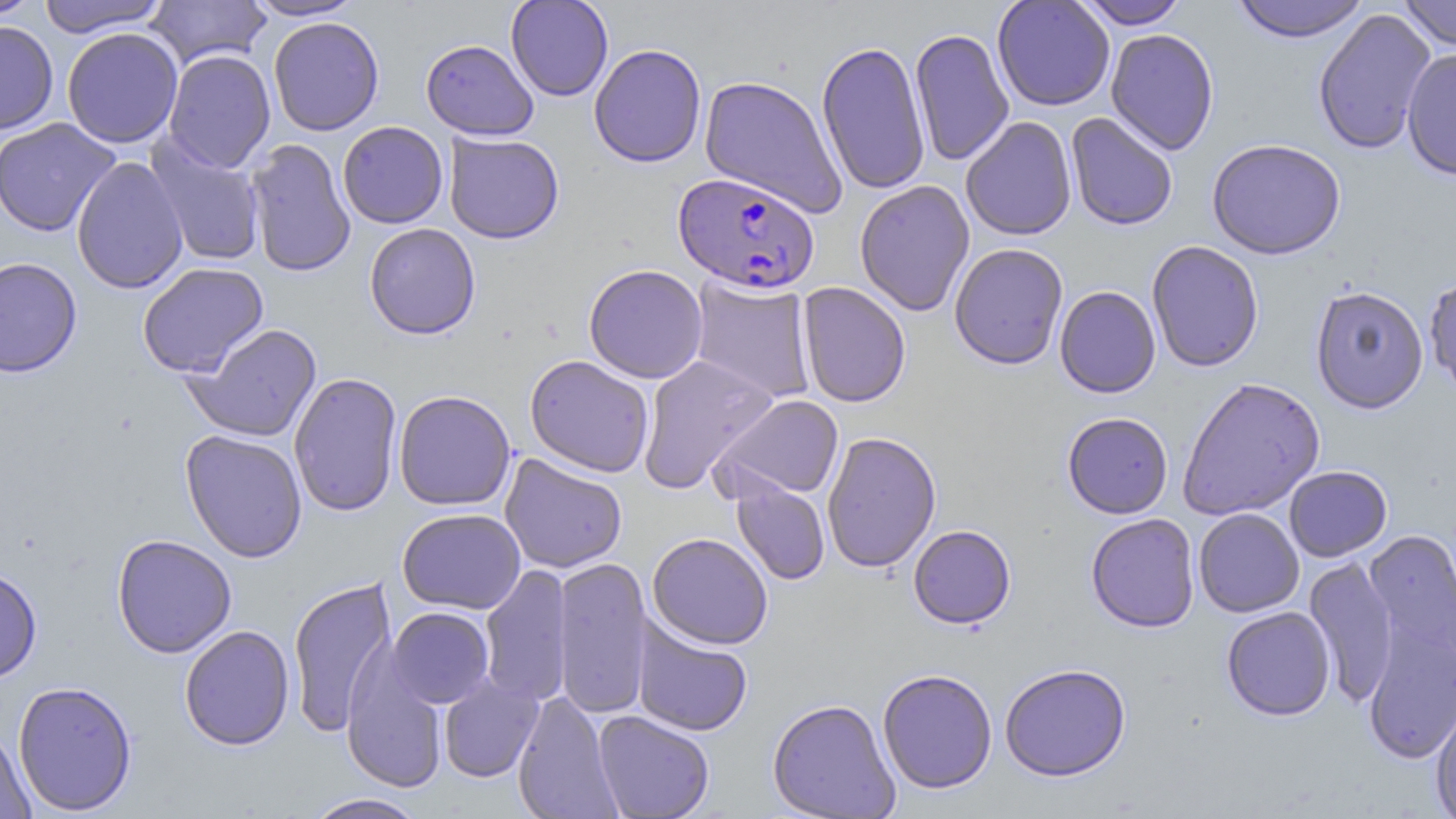
Approximate bounding boxes as (x1, y1, x2, y2) in pixels. Uninfected red blood cell locations: (0, 0, 43, 22), (37, 0, 170, 38), (243, 0, 365, 21), (505, 0, 614, 102), (992, 0, 1115, 111), (1074, 0, 1191, 29), (1230, 0, 1370, 43), (1399, 0, 1456, 50), (146, 1, 271, 70), (1313, 8, 1436, 155), (268, 17, 384, 136), (0, 21, 58, 135), (62, 27, 183, 149), (909, 27, 1015, 167), (1105, 28, 1220, 155), (420, 39, 539, 140), (817, 40, 931, 197), (589, 43, 707, 168), (1401, 48, 1456, 180), (163, 49, 276, 173), (699, 74, 847, 218), (1065, 112, 1178, 231), (959, 116, 1077, 241), (0, 118, 120, 237), (337, 121, 449, 229), (443, 132, 565, 244), (145, 135, 266, 268), (245, 138, 356, 278), (1207, 138, 1346, 260), (71, 156, 189, 295), (854, 180, 975, 317), (364, 223, 481, 339), (1146, 241, 1264, 372), (949, 243, 1069, 370), (0, 256, 82, 378), (137, 262, 269, 377), (583, 264, 708, 383), (1424, 274, 1456, 398), (687, 276, 818, 404), (797, 282, 911, 408), (1054, 285, 1161, 398), (1310, 285, 1429, 414), (182, 323, 323, 442), (524, 354, 655, 477), (636, 354, 778, 494), (288, 372, 402, 517), (1177, 377, 1325, 521), (393, 389, 516, 511), (712, 394, 845, 502), (1062, 411, 1173, 519), (180, 430, 308, 563), (822, 431, 942, 573), (499, 453, 628, 573), (1284, 465, 1393, 562), (731, 478, 830, 586), (397, 508, 526, 614), (1193, 508, 1304, 617), (1085, 513, 1200, 632), (908, 525, 1016, 629), (1362, 525, 1456, 677), (646, 532, 774, 649), (112, 533, 237, 658), (552, 556, 653, 720), (1304, 557, 1399, 708), (479, 563, 571, 708), (0, 565, 42, 683), (287, 576, 397, 738), (1221, 606, 1335, 721), (387, 607, 494, 708), (631, 614, 753, 737), (1362, 618, 1456, 766), (179, 625, 294, 750), (341, 647, 447, 794), (999, 663, 1132, 781), (877, 668, 997, 794), (438, 676, 543, 783), (13, 680, 138, 815), (512, 691, 622, 819), (1431, 695, 1456, 818), (767, 698, 901, 818), (593, 711, 714, 818), (0, 727, 36, 819), (303, 793, 429, 819). Plasmodium falciparum-infected red blood cell locations: (673, 171, 821, 293). Slide-level diagnosis: Plasmodium falciparum. Image is 1456×819 pixels. May-Grünwald-Giemsa stain. Optical microscopy. Single field of view. Thin blood film. 1000x magnification.